Classify this cell by malaria status.
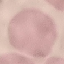

Uninfected.

{
  "stain": "Giemsa",
  "image_type": "automatically extracted cell patch, resized to 64 × 64 pixels",
  "preparation": "thin blood film",
  "capture": "smartphone camera at the microscope eyepiece"
}